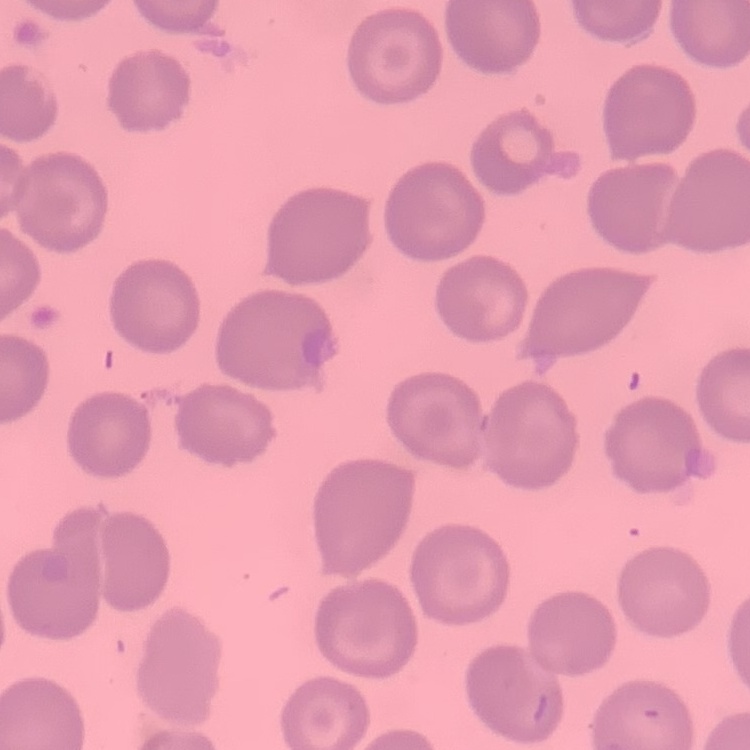
Summary:
  - Red blood cell morphology: no rouleaux formation
  - Preparation: thin blood smear
  - Image type: square crop of a larger photomicrograph
  - Stain: Field's or Giemsa